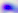
Summary:
  - Identification: Toxoplasma gondii
  - Modality: micrograph
  - Magnification: 400x